Report the malaria status of this cell.
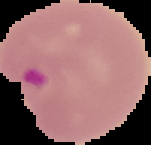
It is parasitized.

Summary:
  - Image size: 151×145 pixels
  - Image type: segmented cell region on a black background
  - Preparation: thin blood smear